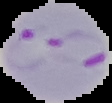
Malaria status: parasitized. Cell region segmented out of the field of view; the surrounding area is masked to black. From a thin blood film. Image is 112×103 pixels.